Comment on the morphology of the erythrocytes.
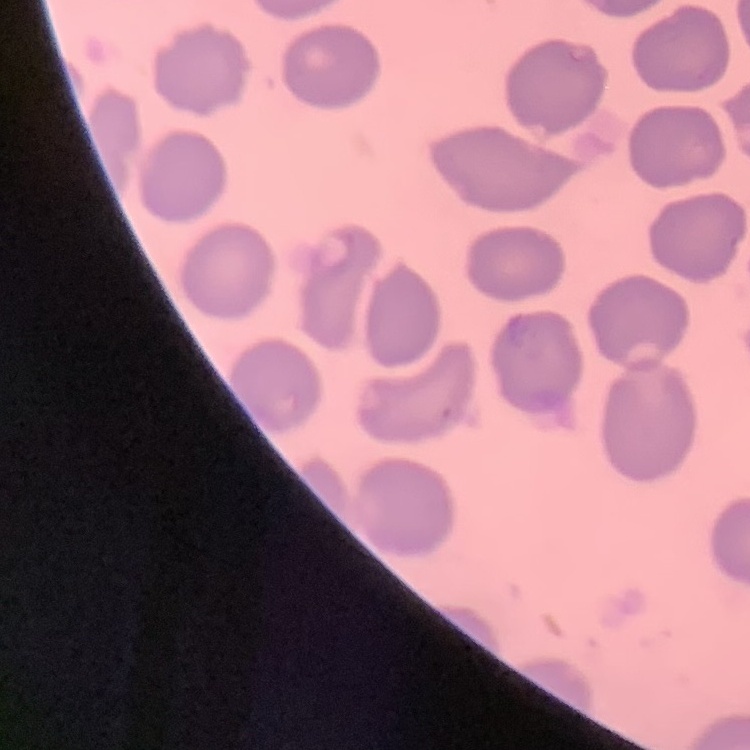

No rouleaux formation.

Summary:
  - Image type: square crop of a larger photomicrograph
  - Preparation: thin peripheral smear
  - Stain: Field's or Giemsa